Give the extent of all Plasmodium falciparum-infected red blood cells.
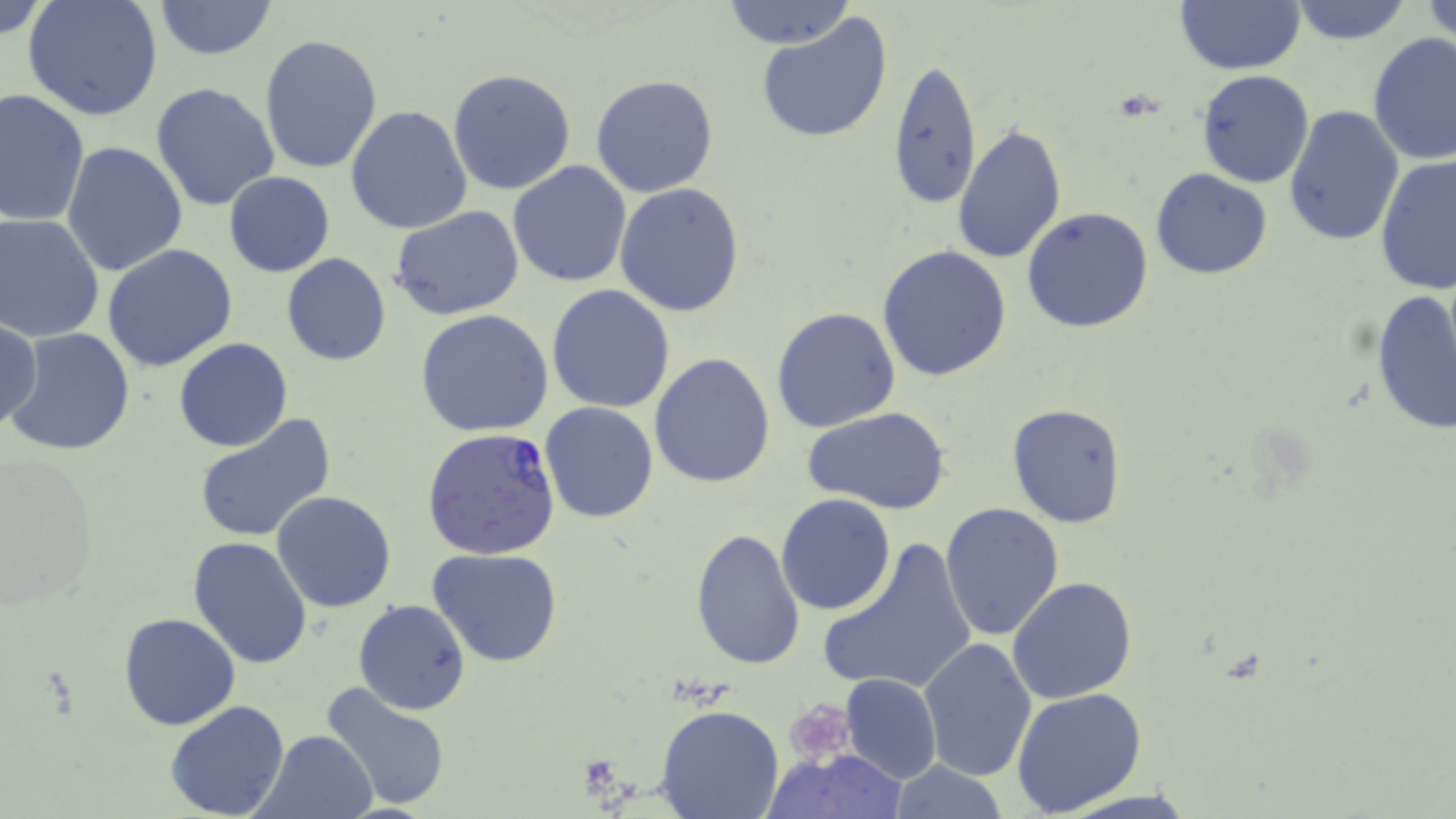
Approximate bounding boxes as (x1,y1)-(x2,y2) corner pairs in pixels.
Plasmodium falciparum-infected red blood cells: (423,426)-(561,562).

Platelet locations: (784,699)-(856,769). Uninfected red blood cell locations: (0,0)-(55,45), (23,0)-(163,122), (718,0)-(857,50), (1421,0)-(1455,45), (151,1)-(278,59), (1174,1)-(1307,73), (1286,1)-(1414,46), (757,14)-(894,144), (1367,32)-(1456,166), (259,34)-(384,176), (888,59)-(982,213), (447,68)-(577,196), (1195,70)-(1315,188), (590,74)-(719,198), (150,82)-(280,214), (0,86)-(90,228), (346,105)-(473,233), (1282,105)-(1404,250), (953,124)-(1067,266), (61,141)-(188,277), (1375,153)-(1455,293), (508,162)-(632,286), (1150,168)-(1273,279), (223,172)-(334,277), (615,183)-(745,318), (389,205)-(525,320), (1022,207)-(1154,333), (0,214)-(104,343), (102,244)-(237,372), (877,245)-(1012,382), (281,253)-(392,366), (547,285)-(675,413), (1371,289)-(1455,436), (420,298)-(675,424), (770,306)-(900,432), (415,309)-(553,436), (1,318)-(43,436), (3,328)-(137,457), (173,338)-(295,453), (650,352)-(778,488), (540,402)-(659,524), (1006,402)-(1129,529), (806,406)-(951,515), (193,413)-(336,543), (0,452)-(100,609), (273,490)-(397,611), (775,492)-(896,616), (940,503)-(1065,642), (689,527)-(805,671), (187,535)-(312,670), (817,536)-(978,698), (429,548)-(564,667), (1007,576)-(1138,704), (354,599)-(471,714), (117,612)-(241,731), (916,636)-(1036,783), (840,674)-(942,784), (319,681)-(453,810), (1011,688)-(1147,815), (166,701)-(290,819), (656,702)-(784,819), (253,729)-(377,817), (772,748)-(905,819), (889,759)-(1010,818). Slide-level diagnosis: Plasmodium falciparum. Thin blood smear. One field of a larger specimen. Optical microscopy. Image is 1456×819 pixels. May-Grünwald-Giemsa-stained preparation. 1000x magnification.